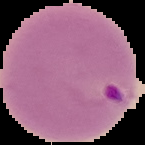

Summary:
  - Image type: cell region segmented out of the field of view; surrounding area masked to black
  - Result: malaria parasites identified
  - Image size: 145×145 pixels
  - Preparation: thin blood film